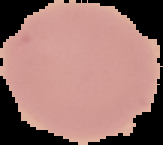

image size = 163×145 pixels
preparation = thin blood film
malaria status = uninfected
image type = cell region segmented out of the field of view; surrounding area masked to black